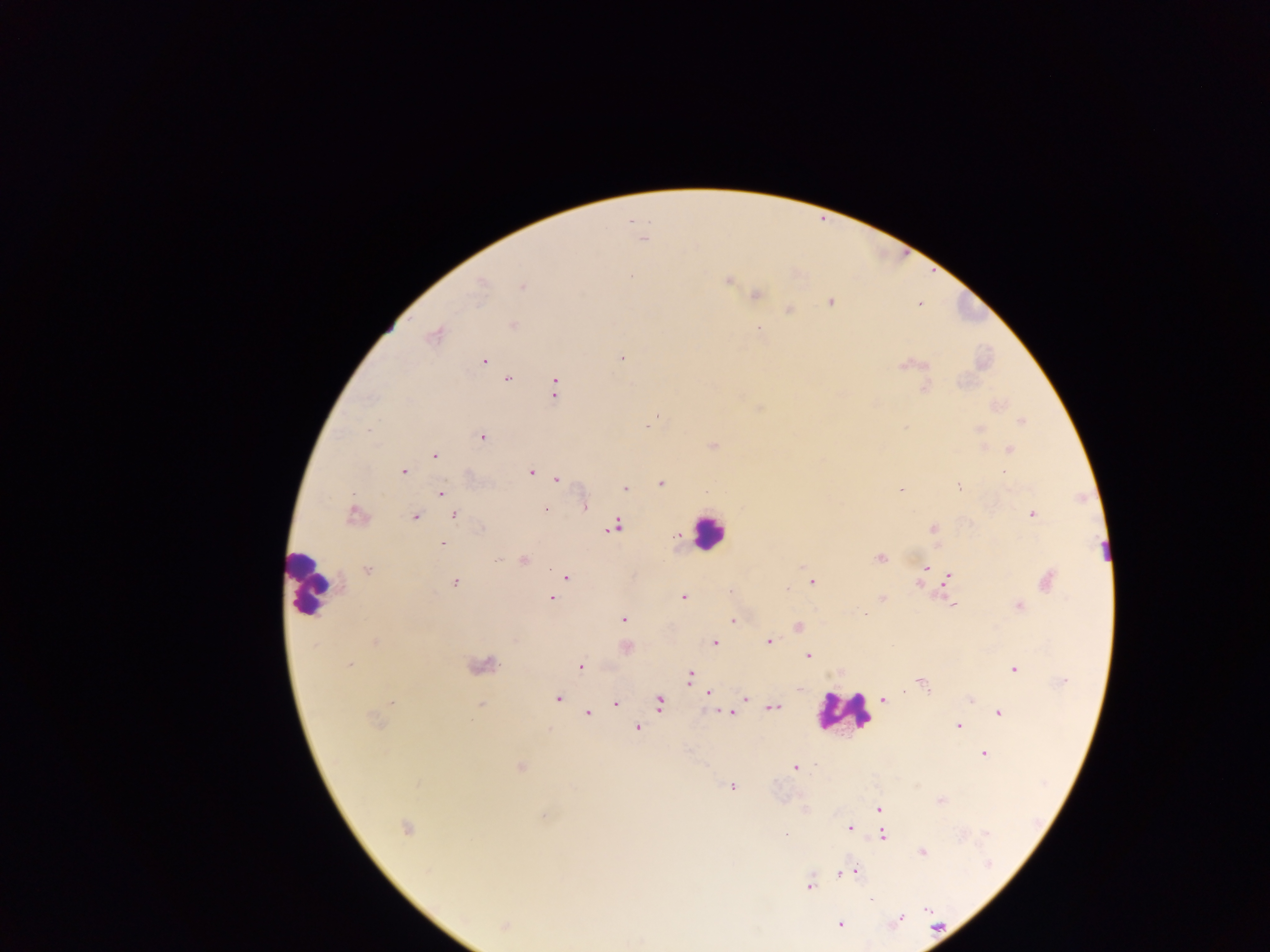
leukocyte_locations: 'approximate centers as {x, y} in pixels: {708, 532}, {309, 582}, {843, 712}'
plasmodium_parasite_locations: 'approximate centers as {x, y} in pixels: {643, 239}, {631, 276}, {728, 281}, {481, 285}, {522, 287}, {756, 295}, {831, 302}, {789, 310}, {512, 325}, {757, 328}, {434, 336}, {621, 357}, {484, 360}, {902, 366}, {507, 379}, {555, 388}, {924, 388}, {655, 417}, {1021, 421}, {979, 429}, {482, 437}, {713, 446}, {1010, 450}, {434, 455}, {404, 472}, {530, 472}, {557, 479}, {661, 484}, {959, 485}, {625, 488}, {900, 490}, {440, 493}, {585, 506}, {545, 509}, {454, 515}, {1032, 515}, {354, 516}, {415, 516}, {615, 525}, {482, 529}, {933, 529}, {442, 545}, {880, 558}, {523, 561}, {927, 568}, {367, 571}, {923, 574}, {948, 576}, {566, 577}, {1047, 580}, {812, 581}, {455, 583}, {919, 584}, {787, 588}, {683, 596}, {552, 597}, {882, 597}, {954, 605}, {1019, 606}, {866, 614}, {623, 619}, {733, 621}, {798, 627}, {769, 641}, {375, 642}, {715, 643}, {808, 655}, {349, 665}, {580, 667}, {1013, 669}, {690, 677}, {922, 684}, {708, 692}, {557, 698}, {746, 698}, {971, 699}, {884, 700}, {659, 703}, {393, 704}, {616, 704}, {480, 705}, {774, 707}, {588, 713}, {730, 713}, {999, 713}, {374, 720}, {959, 726}, {638, 728}, {983, 755}, {520, 767}, {795, 768}, {731, 786}, {940, 800}, {879, 809}, {542, 816}, {406, 827}, {849, 828}, {785, 833}, {883, 835}, {922, 853}, {855, 870}, {841, 872}, {810, 886}, {871, 899}, {927, 910}, {900, 919}, {840, 924}, {504, 925}'
capture: mobile-phone photograph through a microscope
country: Ghana
preparation: thick blood smear
field_of_view: single
image_size: 1270×952 pixels